Point out each Plasmodium parasite.
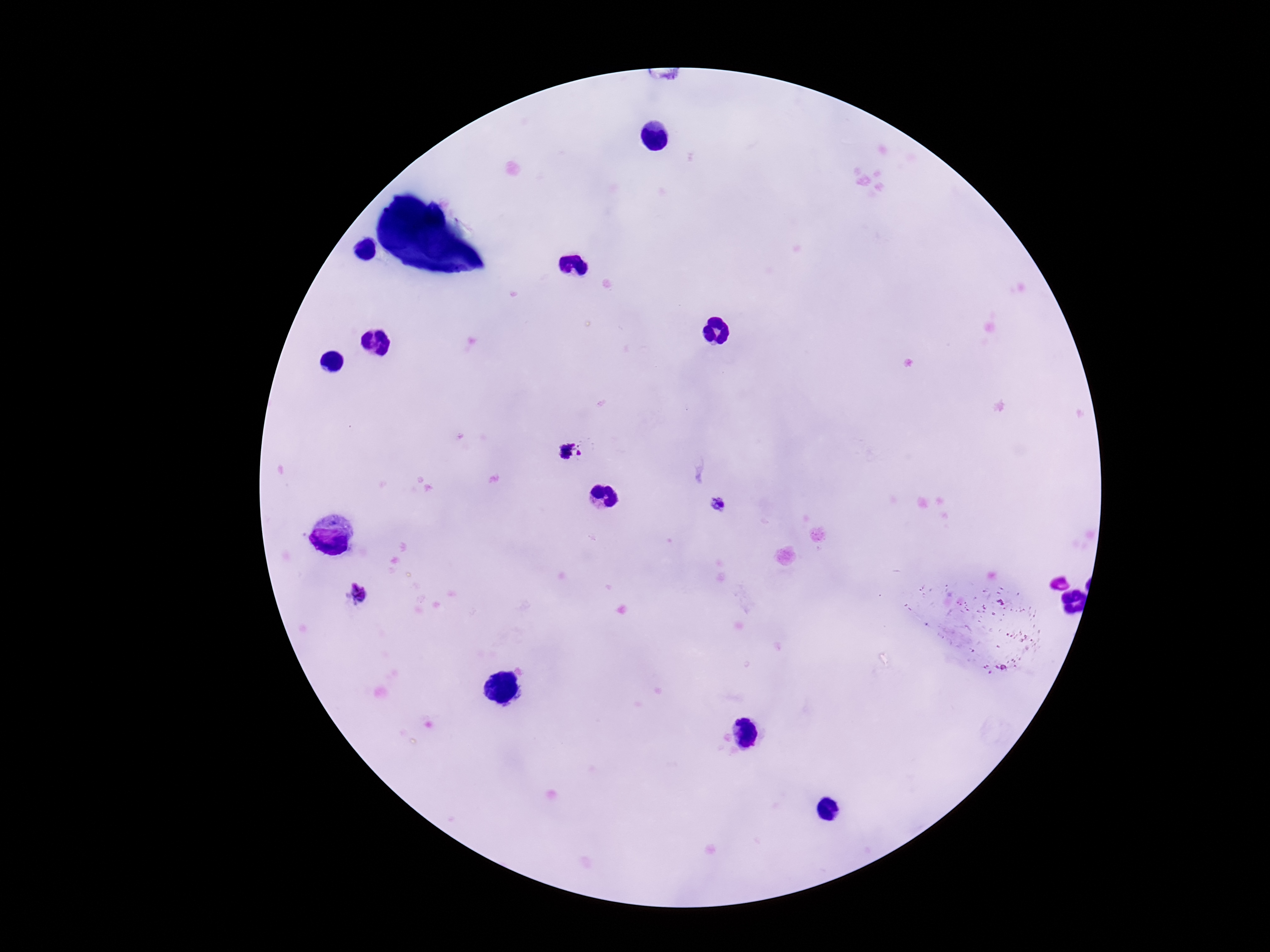

Approximate centers as {x, y} in pixels.
Plasmodium parasites: {571, 452}, {718, 504}, {358, 595}.

One field from this slide. Giemsa stain. Patient malaria status: infected. Photographed through the microscope eyepiece with a smartphone camera. Thick peripheral-blood smear. Image is 1270×952 pixels. 100x magnification.